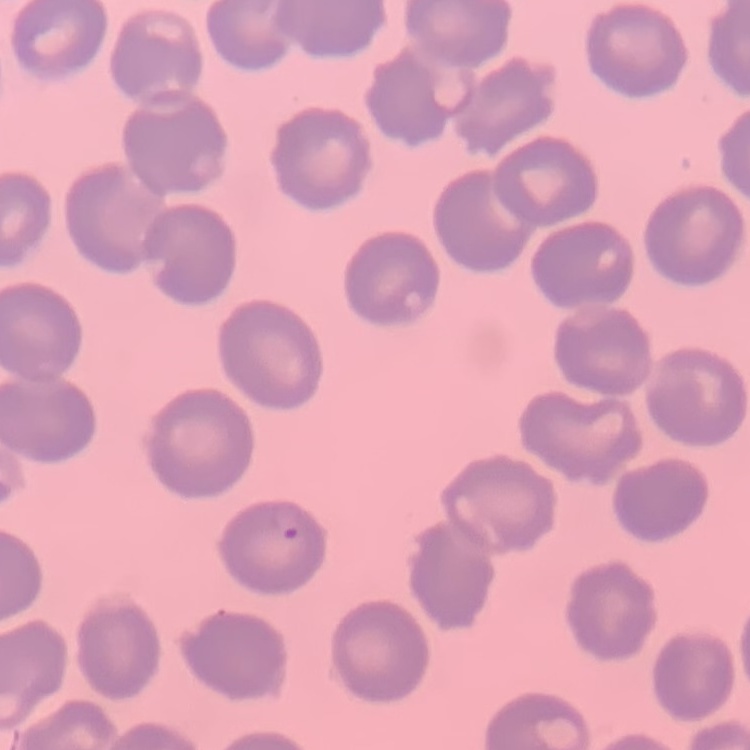 The erythrocytes exhibit no rouleaux formation. One tile cut from a larger photomicrograph. Thin blood film. Field's or Giemsa stain.